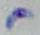

Summary:
  - Identification: Toxoplasma gondii
  - Modality: micrograph
  - Magnification: 1000x